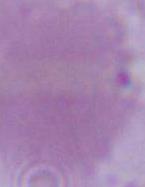
magnification: 1000x
modality: photomicrograph
identification: erythrocyte